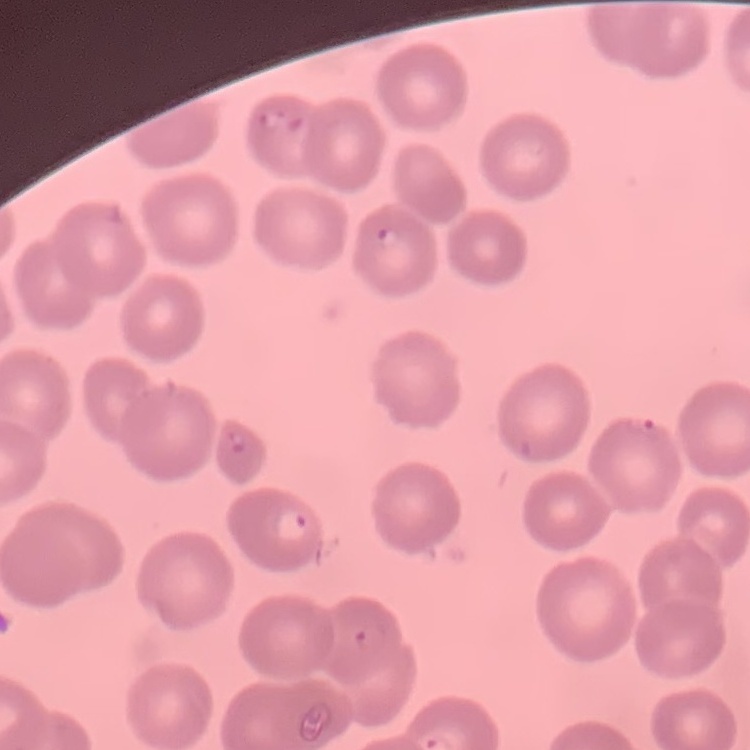

The red blood cells show no rouleaux formation. One tile cut from a larger photomicrograph. Thin peripheral smear. Field's or Giemsa stain.